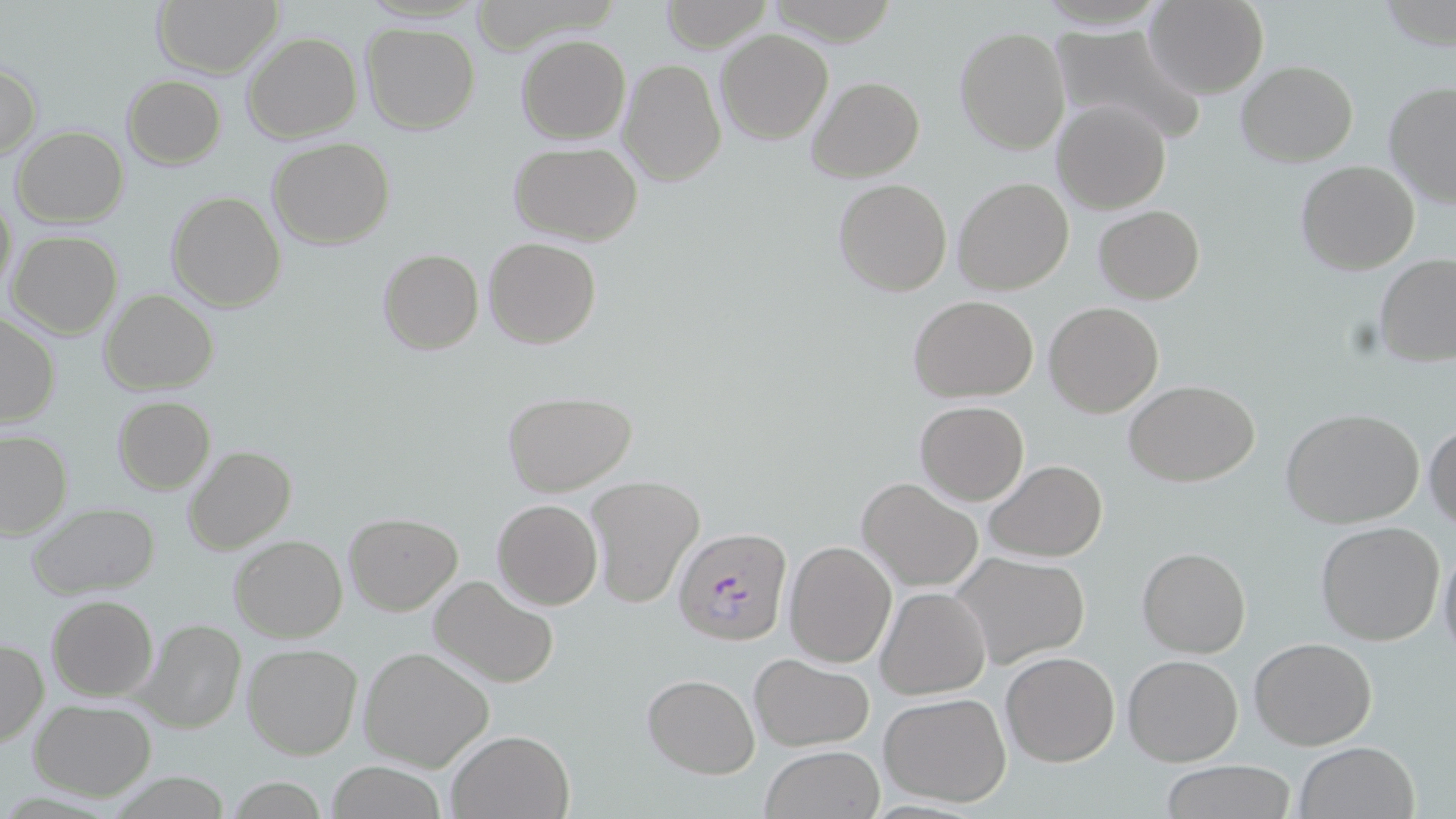 Approximate bounding boxes as named x1/y1/x2/y2 corners in pixels. Uninfected red blood cell locations: (x1=152, y1=0, x2=284, y2=77), (x1=658, y1=0, x2=772, y2=52), (x1=1146, y1=0, x2=1269, y2=98), (x1=360, y1=23, x2=480, y2=134), (x1=1047, y1=26, x2=1204, y2=145), (x1=955, y1=28, x2=1070, y2=153), (x1=717, y1=29, x2=831, y2=144), (x1=242, y1=31, x2=362, y2=143), (x1=517, y1=34, x2=630, y2=144), (x1=618, y1=58, x2=726, y2=187), (x1=1236, y1=61, x2=1358, y2=166), (x1=0, y1=63, x2=41, y2=157), (x1=121, y1=75, x2=226, y2=168), (x1=807, y1=75, x2=924, y2=182), (x1=1381, y1=81, x2=1456, y2=208), (x1=1052, y1=98, x2=1170, y2=213), (x1=11, y1=127, x2=128, y2=226), (x1=267, y1=136, x2=395, y2=250), (x1=509, y1=143, x2=641, y2=243), (x1=1295, y1=159, x2=1420, y2=274), (x1=953, y1=176, x2=1074, y2=296), (x1=832, y1=179, x2=953, y2=297), (x1=1, y1=189, x2=17, y2=304), (x1=167, y1=192, x2=285, y2=311), (x1=1094, y1=203, x2=1205, y2=303), (x1=8, y1=230, x2=123, y2=340), (x1=482, y1=238, x2=601, y2=351), (x1=377, y1=248, x2=484, y2=354), (x1=1374, y1=254, x2=1456, y2=367), (x1=99, y1=289, x2=218, y2=394), (x1=907, y1=293, x2=1039, y2=401), (x1=1045, y1=301, x2=1163, y2=417), (x1=0, y1=313, x2=60, y2=427), (x1=1124, y1=380, x2=1262, y2=487), (x1=502, y1=391, x2=635, y2=494), (x1=112, y1=397, x2=216, y2=493), (x1=914, y1=400, x2=1029, y2=505), (x1=1281, y1=408, x2=1427, y2=529), (x1=1424, y1=423, x2=1456, y2=529), (x1=1, y1=429, x2=71, y2=537), (x1=183, y1=446, x2=297, y2=555), (x1=985, y1=459, x2=1107, y2=563), (x1=584, y1=475, x2=703, y2=607), (x1=857, y1=476, x2=983, y2=589), (x1=842, y1=479, x2=981, y2=693), (x1=491, y1=498, x2=603, y2=609), (x1=26, y1=502, x2=160, y2=599), (x1=343, y1=511, x2=464, y2=616), (x1=1315, y1=521, x2=1446, y2=647), (x1=227, y1=536, x2=347, y2=642), (x1=785, y1=539, x2=897, y2=668), (x1=1137, y1=545, x2=1251, y2=658), (x1=1437, y1=545, x2=1456, y2=665), (x1=949, y1=552, x2=1091, y2=669), (x1=428, y1=574, x2=560, y2=687), (x1=877, y1=586, x2=991, y2=699), (x1=47, y1=595, x2=158, y2=701), (x1=135, y1=619, x2=245, y2=735), (x1=1249, y1=638, x2=1377, y2=751), (x1=1, y1=640, x2=47, y2=746), (x1=242, y1=644, x2=363, y2=760), (x1=359, y1=646, x2=493, y2=772), (x1=1000, y1=650, x2=1120, y2=767), (x1=747, y1=653, x2=875, y2=750), (x1=1122, y1=654, x2=1244, y2=766), (x1=642, y1=671, x2=760, y2=779), (x1=879, y1=692, x2=1012, y2=808), (x1=28, y1=700, x2=156, y2=800), (x1=448, y1=727, x2=576, y2=819), (x1=1293, y1=740, x2=1420, y2=819), (x1=759, y1=745, x2=885, y2=819), (x1=1158, y1=760, x2=1300, y2=818), (x1=320, y1=762, x2=452, y2=818). Plasmodium falciparum-infected red blood cell locations: (x1=672, y1=525, x2=792, y2=644). Slide-level diagnosis: Plasmodium falciparum. Optical microscopy. Captured at 1000x magnification. Thin blood smear. Image is 1456×819 pixels. One field of a larger specimen. May-Grünwald-Giemsa stain.